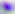

modality = micrograph
identification = Toxoplasma gondii
magnification = 400x